Give the position of every leukocyte visible.
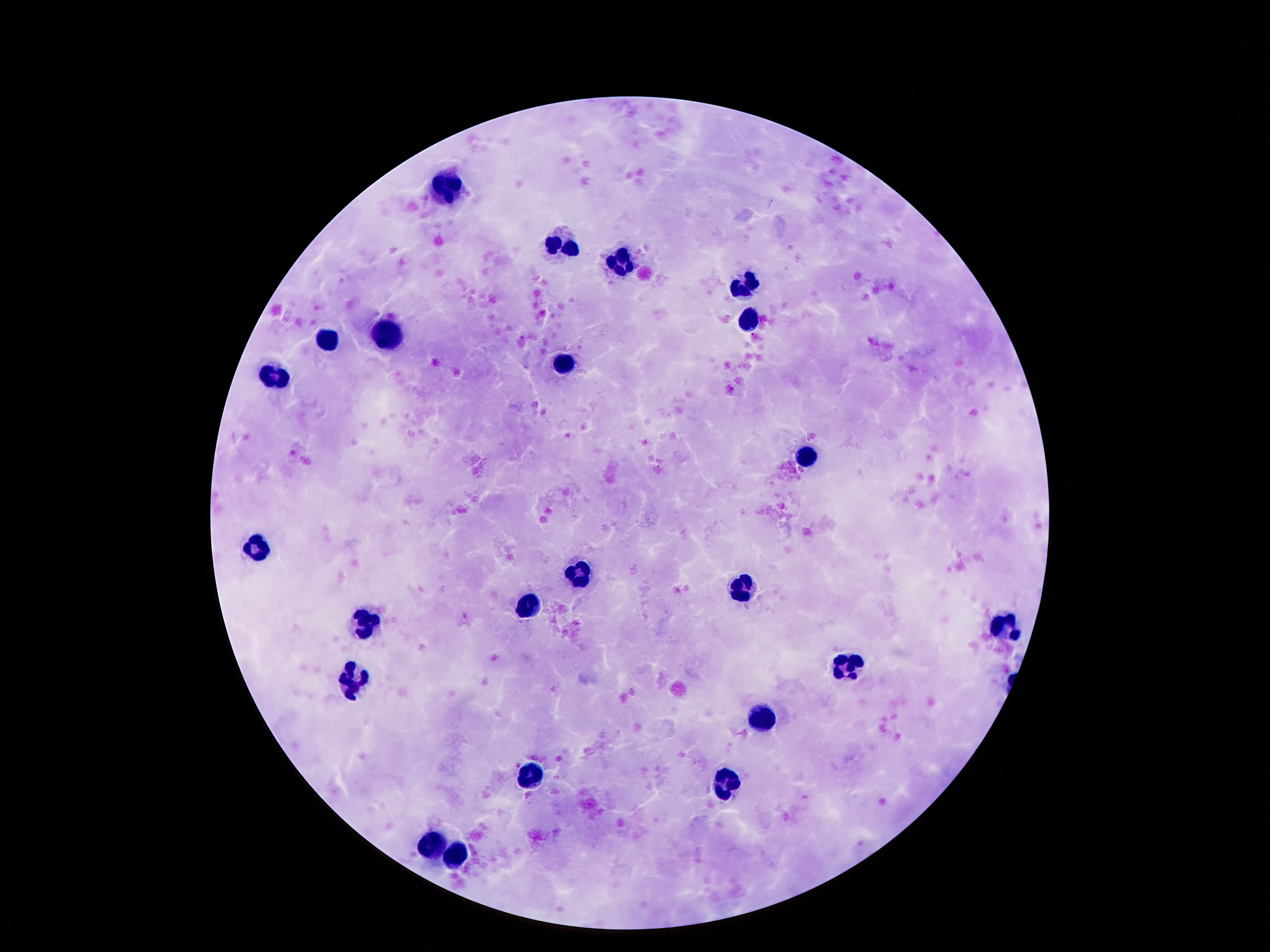
Approximate centers as (x, y) in pixels.
Leukocytes: (449, 186), (563, 246), (622, 263), (746, 282), (746, 318), (392, 332), (329, 339), (565, 364), (275, 374), (806, 459), (257, 543), (578, 575), (742, 585), (526, 603), (368, 621), (1003, 627), (846, 667), (352, 681), (762, 715), (529, 773), (726, 783), (433, 846), (456, 854).

Summary:
  - Capture: smartphone camera through the microscope eyepiece
  - Patient malaria status: negative
  - Image size: 1270×952 pixels
  - Preparation: thick peripheral-blood smear
  - Stain: Giemsa
  - Field of view: one from this slide
  - Magnification: 100x